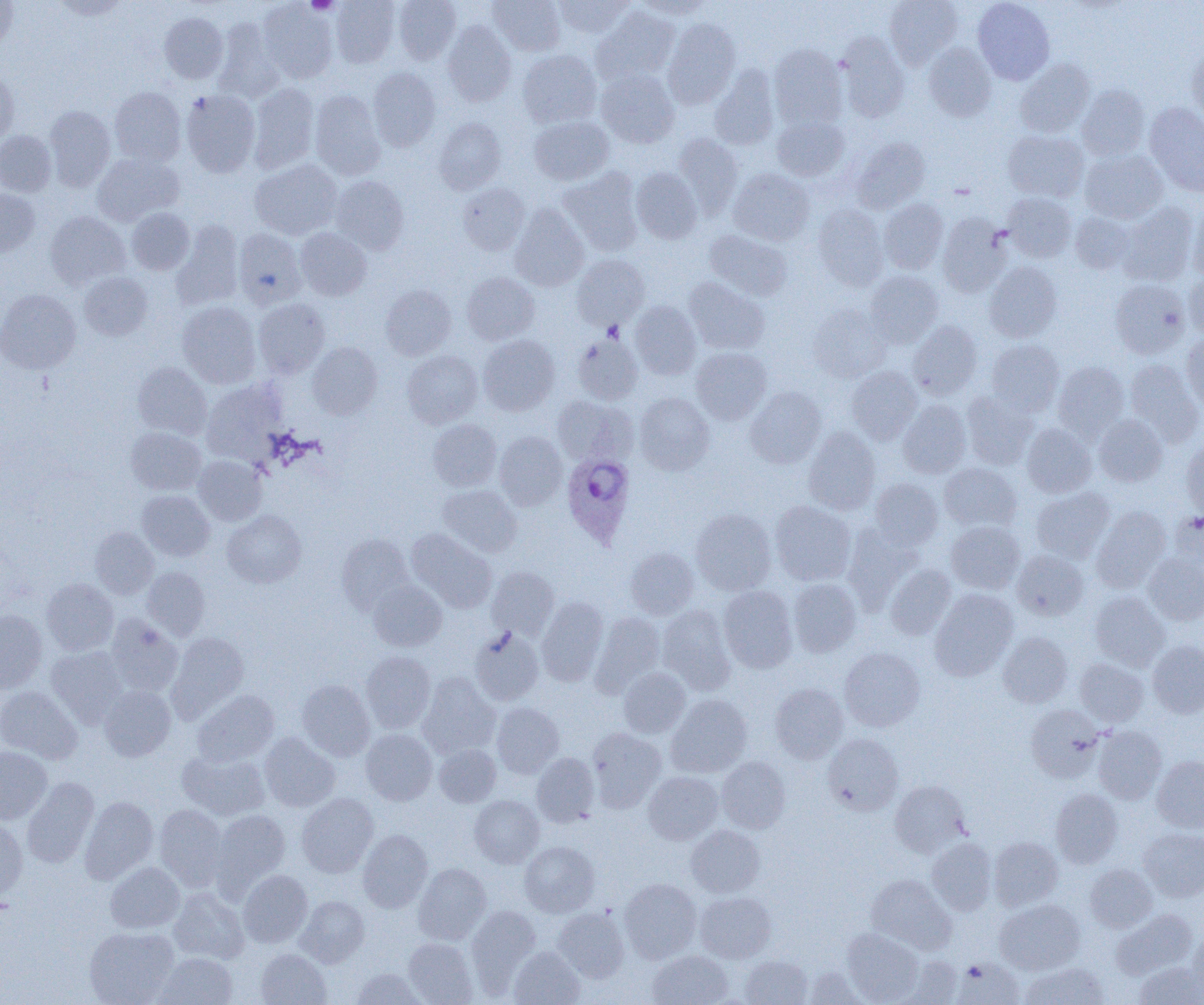
Approximate bounding boxes as (x1, y1, x2, y2) in pixels. Platelet locations: (306, 0, 339, 15). Plasmodium ovale-infected red blood cell locations: (561, 452, 635, 548). Uninfected red blood cell locations: (49, 0, 131, 20), (330, 0, 399, 68), (393, 0, 461, 65), (488, 0, 565, 55), (554, 0, 634, 38), (634, 0, 713, 18), (884, 0, 962, 68), (972, 0, 1055, 84), (0, 1, 20, 51), (258, 1, 337, 83), (593, 6, 679, 85), (159, 12, 228, 83), (663, 18, 740, 108), (213, 20, 284, 103), (442, 21, 516, 106), (836, 33, 910, 123), (923, 43, 996, 121), (769, 44, 848, 129), (1187, 47, 1204, 126), (517, 50, 601, 128), (1016, 59, 1095, 137), (709, 66, 779, 151), (368, 67, 440, 151), (596, 68, 679, 148), (0, 71, 18, 147), (248, 83, 319, 174), (1077, 85, 1150, 160), (109, 87, 186, 165), (181, 90, 260, 177), (309, 90, 385, 179), (1144, 102, 1204, 196), (44, 105, 115, 191), (529, 116, 614, 185), (772, 116, 849, 181), (434, 117, 506, 194), (1003, 130, 1088, 202), (0, 131, 56, 196), (673, 134, 743, 217), (851, 137, 930, 213), (1080, 149, 1168, 223), (92, 152, 183, 225), (250, 159, 342, 240), (631, 167, 702, 243), (559, 168, 643, 256), (728, 168, 814, 246), (330, 175, 409, 255), (457, 183, 529, 254), (0, 188, 39, 257), (1002, 193, 1077, 262), (879, 198, 949, 274), (1187, 200, 1204, 280), (1117, 202, 1198, 285), (813, 204, 888, 291), (510, 205, 589, 291), (127, 208, 194, 274), (45, 211, 130, 290), (1070, 212, 1136, 273), (937, 213, 1011, 297), (172, 221, 244, 310), (233, 228, 306, 308), (295, 228, 371, 301), (704, 229, 793, 300), (572, 255, 649, 330), (985, 262, 1062, 342), (1184, 269, 1204, 340), (865, 271, 943, 347), (79, 272, 153, 340), (461, 272, 540, 345), (684, 277, 769, 354), (1110, 279, 1190, 359), (380, 285, 456, 360), (0, 289, 81, 374), (253, 299, 330, 378), (629, 301, 702, 380), (177, 302, 261, 388), (808, 304, 891, 382), (907, 320, 982, 400), (571, 333, 643, 404), (1181, 333, 1204, 410), (478, 335, 560, 415), (987, 339, 1064, 416), (307, 342, 382, 419), (691, 347, 771, 424), (402, 350, 483, 428), (1124, 360, 1203, 445), (1053, 361, 1130, 440), (132, 362, 212, 439), (846, 366, 922, 444), (201, 380, 287, 463), (745, 387, 827, 468), (961, 391, 1038, 469), (635, 393, 714, 474), (552, 396, 634, 465), (897, 400, 971, 478), (1093, 415, 1168, 486), (428, 419, 501, 490), (1021, 423, 1096, 497), (126, 427, 206, 495), (803, 427, 880, 515), (495, 431, 567, 509), (1181, 437, 1204, 518), (194, 455, 267, 526), (939, 463, 1021, 532), (870, 479, 942, 549), (438, 485, 521, 557), (1031, 488, 1115, 563), (137, 490, 214, 561), (770, 500, 856, 585), (1091, 507, 1171, 592), (690, 508, 776, 595), (222, 510, 306, 587), (1170, 510, 1204, 576), (946, 521, 1025, 594), (843, 523, 922, 611), (90, 527, 159, 599), (407, 527, 497, 613), (336, 534, 413, 613), (626, 548, 699, 619), (1012, 549, 1088, 620), (1143, 553, 1204, 626), (885, 565, 956, 640), (141, 566, 210, 640), (486, 566, 559, 638), (42, 578, 119, 656), (787, 578, 861, 657), (368, 579, 447, 651), (718, 586, 798, 672), (930, 589, 1017, 681), (1089, 591, 1170, 671), (536, 597, 608, 686), (658, 606, 736, 695), (0, 609, 47, 692), (591, 612, 666, 695), (106, 614, 183, 696), (469, 628, 544, 706), (167, 632, 249, 721), (998, 632, 1072, 707), (1147, 640, 1204, 718), (47, 647, 129, 727), (839, 648, 925, 731), (361, 651, 436, 732), (1075, 658, 1148, 727), (619, 667, 691, 738), (417, 673, 501, 759), (297, 680, 375, 761), (770, 683, 848, 763), (99, 685, 176, 761), (0, 687, 82, 764), (192, 690, 278, 766), (666, 694, 752, 777), (491, 702, 564, 778), (1025, 704, 1104, 782), (1093, 726, 1167, 804), (586, 727, 666, 812), (361, 729, 437, 805), (259, 732, 340, 812), (823, 733, 903, 815), (434, 744, 500, 807), (0, 747, 52, 824), (177, 749, 270, 821), (531, 753, 599, 827), (1152, 756, 1204, 832), (716, 757, 791, 833), (643, 772, 723, 844), (22, 777, 99, 868), (890, 780, 970, 856), (1050, 788, 1123, 868), (297, 793, 378, 877), (469, 795, 544, 867), (79, 796, 158, 884), (154, 804, 229, 890), (211, 809, 291, 893), (0, 817, 28, 901), (686, 825, 765, 897), (1138, 827, 1204, 901), (358, 829, 433, 912), (989, 837, 1063, 910), (927, 838, 996, 915), (519, 841, 600, 917), (105, 862, 185, 933), (413, 863, 491, 945), (1085, 864, 1158, 932), (238, 870, 312, 947), (866, 874, 956, 955), (619, 878, 701, 963), (169, 887, 249, 963), (695, 892, 776, 963), (296, 895, 369, 968), (995, 899, 1085, 975), (466, 904, 540, 992), (552, 908, 630, 983), (1112, 909, 1197, 978), (84, 927, 178, 1004), (842, 928, 924, 1004), (1189, 931, 1204, 998), (403, 938, 477, 1005), (509, 946, 584, 1005), (256, 949, 331, 1005), (647, 950, 733, 1005), (155, 952, 237, 1005), (740, 955, 813, 1005), (896, 956, 963, 1005), (953, 957, 1023, 1004), (1020, 962, 1109, 1005), (1134, 962, 1204, 1005), (802, 967, 868, 1004), (350, 968, 428, 1005). Slide-level diagnosis: Plasmodium ovale. Thin blood smear. Image is 1204×1005 pixels. One field of a larger specimen. Optical microscopy. Captured at 1000x magnification.